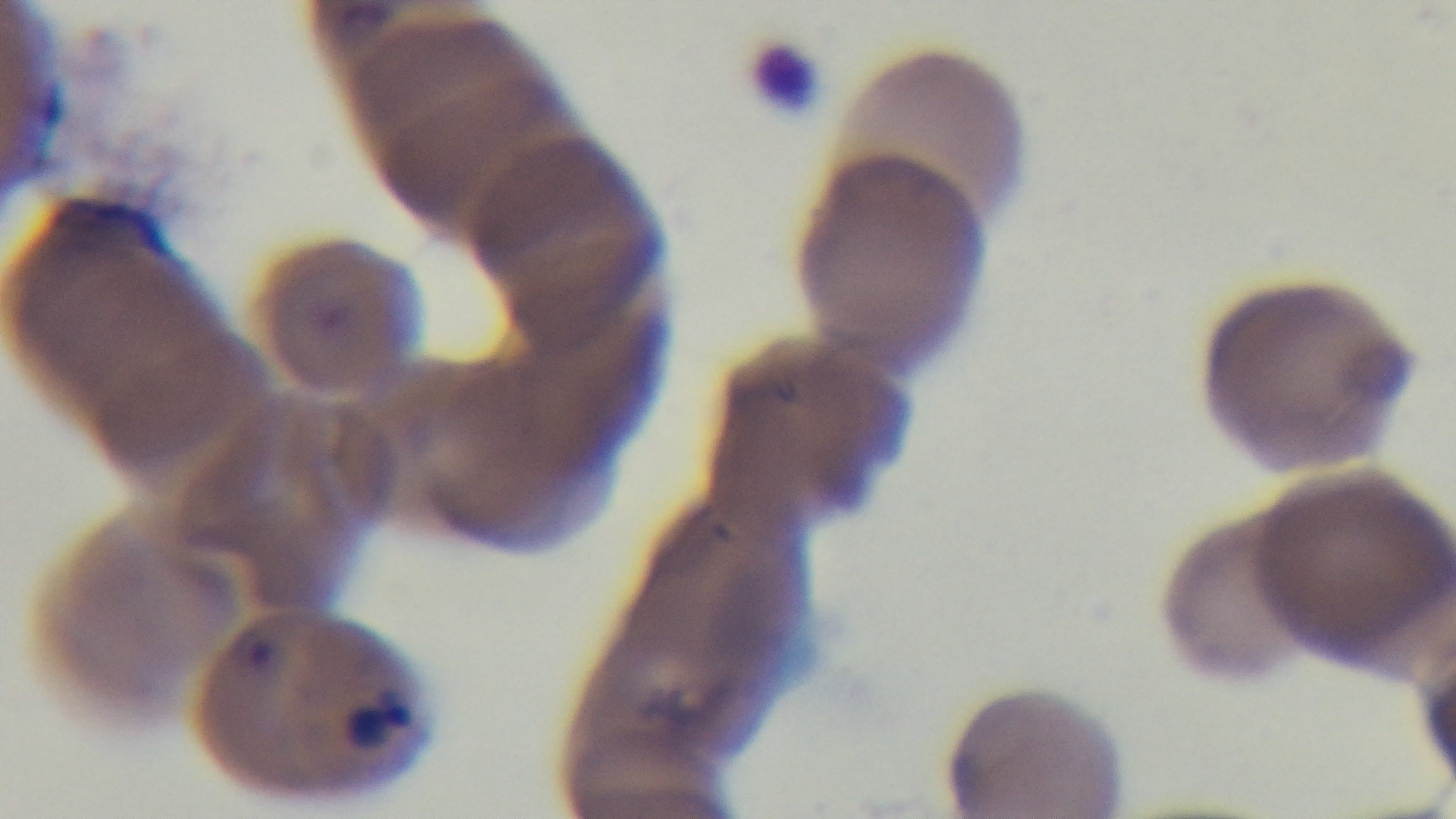
Summary:
  - Preparation: thin smear
  - Stain: Giemsa
  - Capture: mounted 4K digital camera
  - Objective: 100x oil immersion
  - Malaria status: positive
  - Field of view: one from the slide
  - Modality: light microscopy